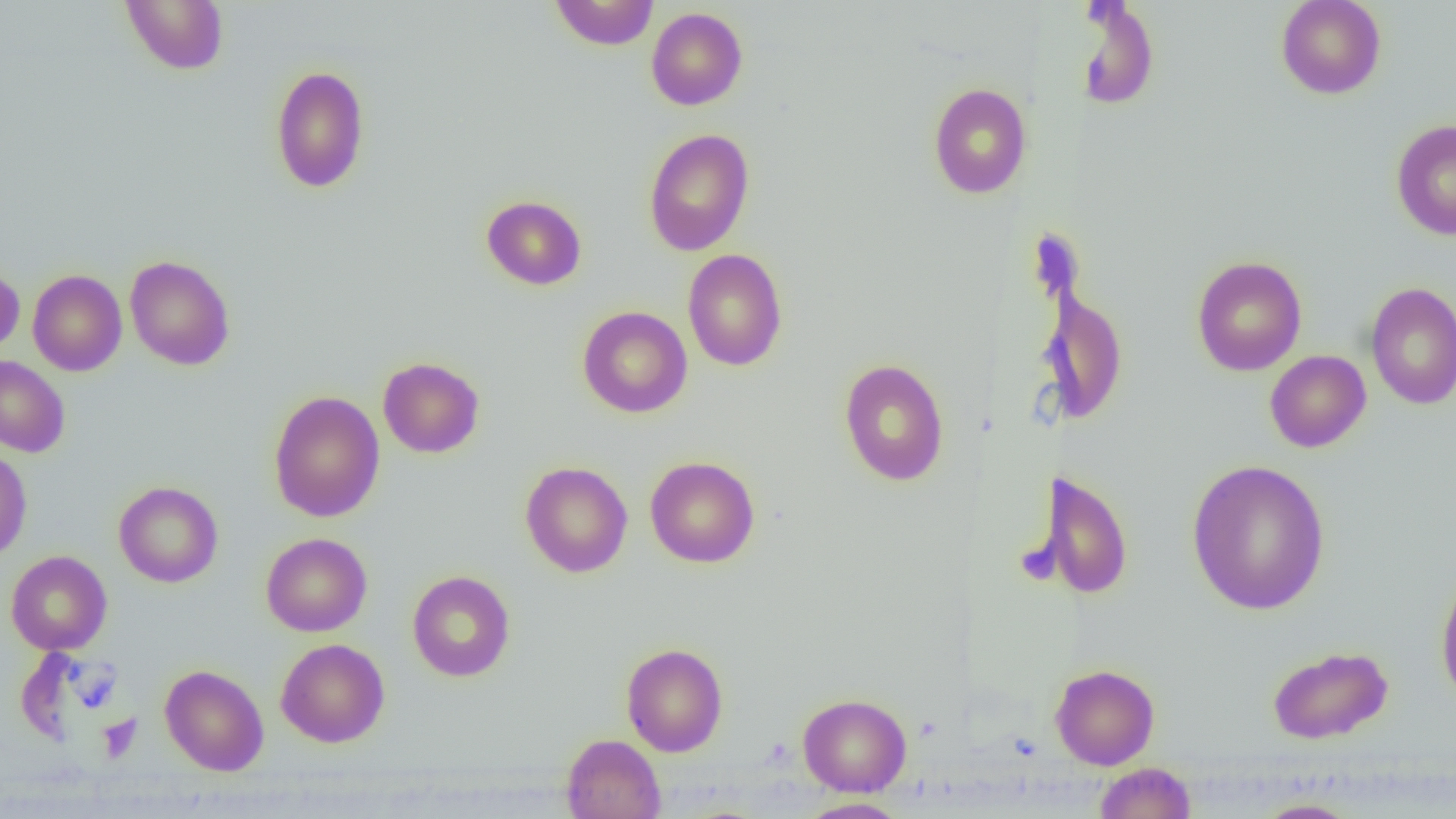
{
  "slide_level_diagnosis": "no evidence of blood parasites",
  "magnification": "1000x",
  "field_of_view": "single",
  "modality": "optical microscopy",
  "uninfected_red_blood_cell_locations": "approximate bounding boxes as (x1,y1)-(x2,y2) corner pairs in pixels: (121,0)-(228,74), (549,0)-(660,50), (1276,0)-(1386,99), (1074,1)-(1160,111), (646,7)-(748,110), (270,65)-(370,193), (928,82)-(1031,199), (1390,118)-(1456,241), (643,128)-(755,256), (481,195)-(587,290), (682,249)-(788,371), (124,255)-(235,370), (1191,256)-(1307,376), (0,264)-(24,355), (27,269)-(127,376), (1365,282)-(1456,410), (1037,287)-(1128,424), (577,305)-(692,418), (1264,350)-(1371,453), (0,355)-(70,457), (377,357)-(485,458), (839,358)-(949,486), (268,390)-(385,522), (0,447)-(32,562), (645,456)-(760,568), (1187,459)-(1330,615), (520,461)-(633,577), (1036,469)-(1133,600), (113,481)-(223,588), (261,532)-(372,636), (6,550)-(112,655), (1435,569)-(1456,709), (407,570)-(515,682), (275,639)-(390,747), (621,643)-(728,756), (1267,645)-(1393,744), (160,664)-(269,776), (1050,664)-(1160,769), (797,693)-(912,797), (561,733)-(666,819), (1094,762)-(1196,819), (797,797)-(910,819), (1252,798)-(1362,818)",
  "image_size": "1456×819 pixels",
  "preparation": "thin blood film"
}